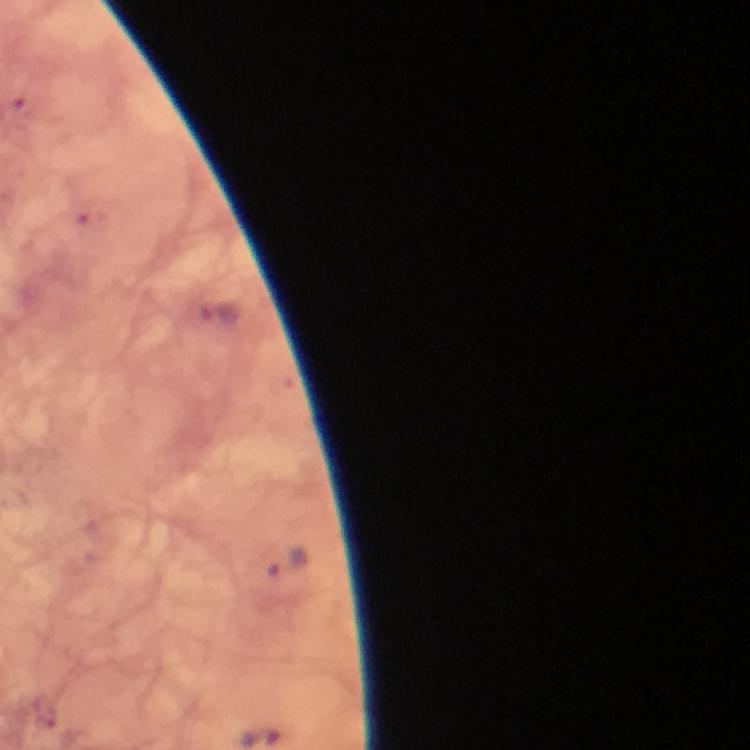

Approximate centers as (x, y) in pixels. Plasmodium parasite locations: (287, 563). Thick blood film. 100x magnification. Image is 750×750 pixels. From a malaria diagnostic workup. Smartphone photograph taken through a microscope. Giemsa-stained preparation. A crop from one field of view. Immersion oil applied.